Name the parasite shown.
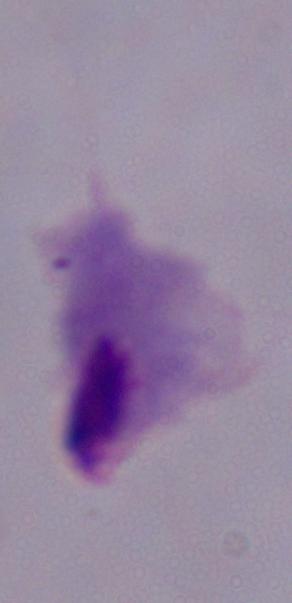
A trichomonad.

1000x magnification. Photomicrograph.